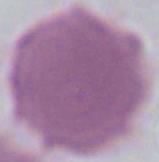
Summary:
  - Identification: erythrocyte
  - Magnification: 1000x
  - Modality: micrograph